Point out each Plasmodium parasite.
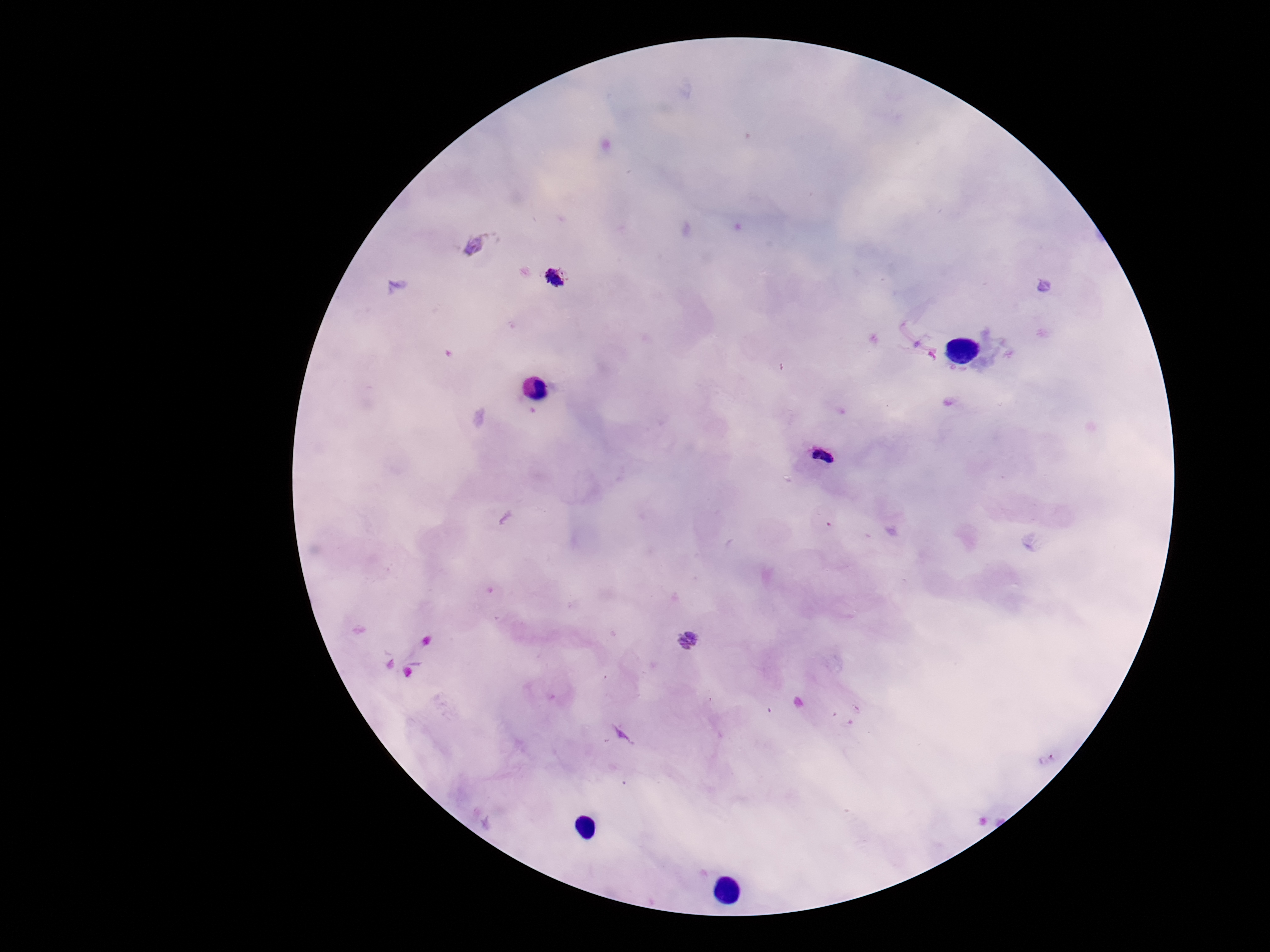

Approximate centers as {x, y} in pixels.
Plasmodium parasites: {475, 245}, {555, 277}, {823, 456}, {687, 641}.

100x magnification. Giemsa-stained preparation. Patient malaria status: positive. Smartphone photograph taken through the microscope eyepiece. Thick peripheral-blood smear. Image is 1270×952 pixels. Single field of view.